Name the parasite shown.
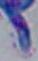
Toxoplasma gondii.

modality = photomicrograph
magnification = 1000x